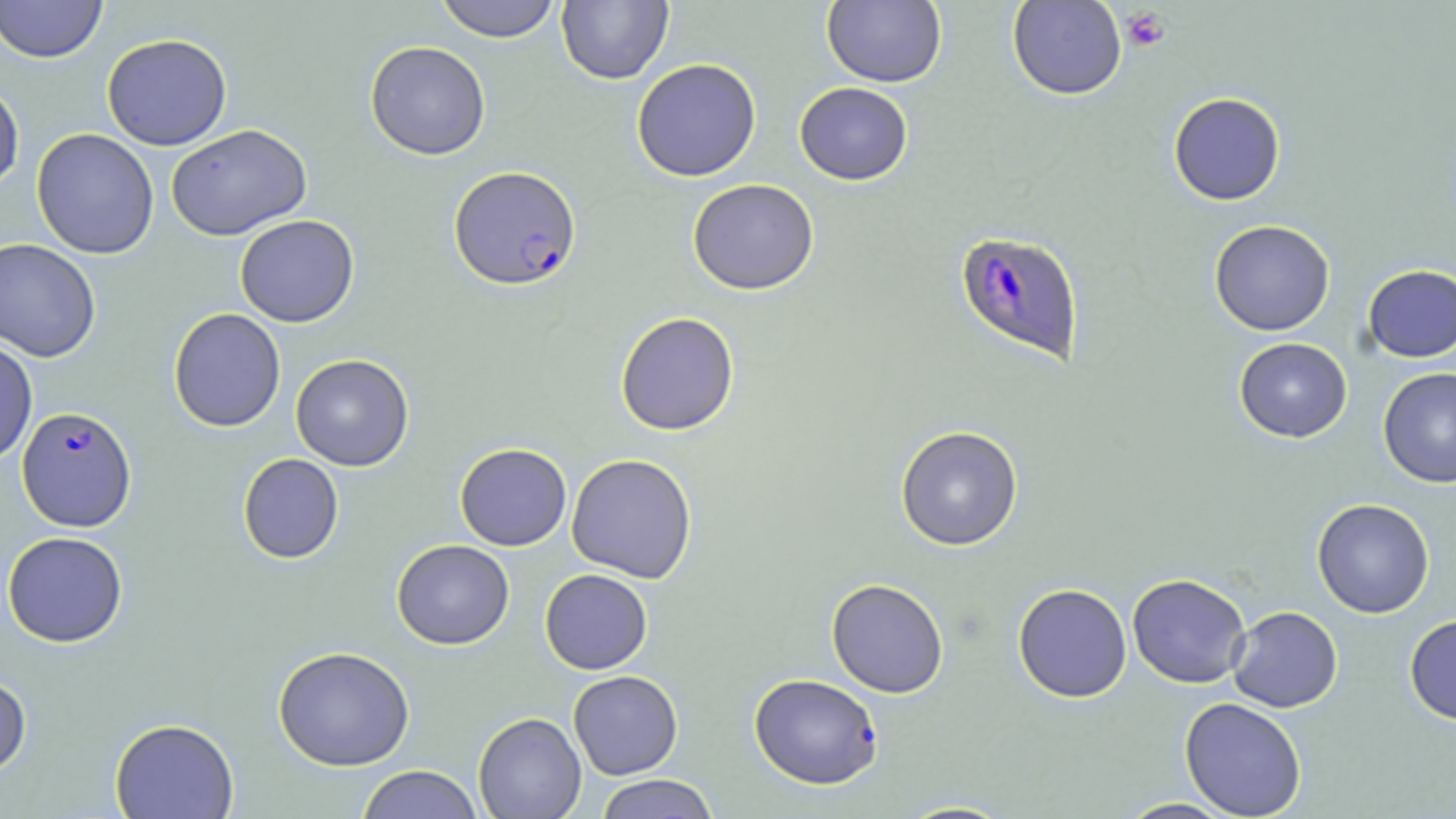

slide-level diagnosis = Plasmodium falciparum
modality = optical microscopy
uninfected red blood cell locations = approximate bounding boxes as (x1, y1, x2, y2) in pixels: (0, 0, 107, 64), (434, 0, 562, 43), (556, 0, 673, 85), (821, 0, 946, 88), (1007, 0, 1126, 100), (102, 33, 232, 150), (365, 41, 491, 160), (631, 58, 762, 182), (0, 81, 25, 194), (794, 82, 913, 185), (1168, 92, 1286, 206), (167, 123, 312, 241), (31, 128, 159, 259), (687, 178, 819, 295), (235, 214, 359, 327), (1208, 219, 1335, 336), (0, 238, 102, 362), (1361, 263, 1456, 363), (168, 308, 286, 432), (615, 311, 740, 436), (1234, 337, 1352, 442), (0, 338, 38, 467), (290, 354, 414, 471), (1378, 368, 1456, 487), (895, 425, 1023, 551), (454, 443, 572, 550), (237, 453, 344, 563), (566, 453, 698, 583), (1311, 498, 1435, 618), (2, 531, 128, 648), (391, 539, 514, 650), (540, 569, 653, 674), (1127, 573, 1251, 688), (826, 578, 949, 698), (1012, 583, 1132, 703), (1227, 606, 1343, 713), (1404, 614, 1456, 724), (273, 645, 415, 771), (568, 670, 683, 779), (0, 673, 32, 778), (1179, 696, 1307, 818), (473, 712, 586, 819), (109, 717, 239, 818), (356, 765, 483, 819), (593, 774, 721, 818), (1114, 797, 1239, 818), (892, 799, 1019, 818)
Plasmodium falciparum-infected red blood cell locations = approximate bounding boxes as (x1, y1, x2, y2) in pixels: (449, 165, 582, 291), (955, 230, 1086, 365), (17, 406, 137, 531), (748, 672, 883, 789)
image size = 1456×819 pixels
preparation = thin blood film
magnification = 1000x
stain = May-Grünwald-Giemsa
field of view = single
platelet locations = approximate bounding boxes as (x1, y1, x2, y2) in pixels: (1120, 6, 1171, 52)